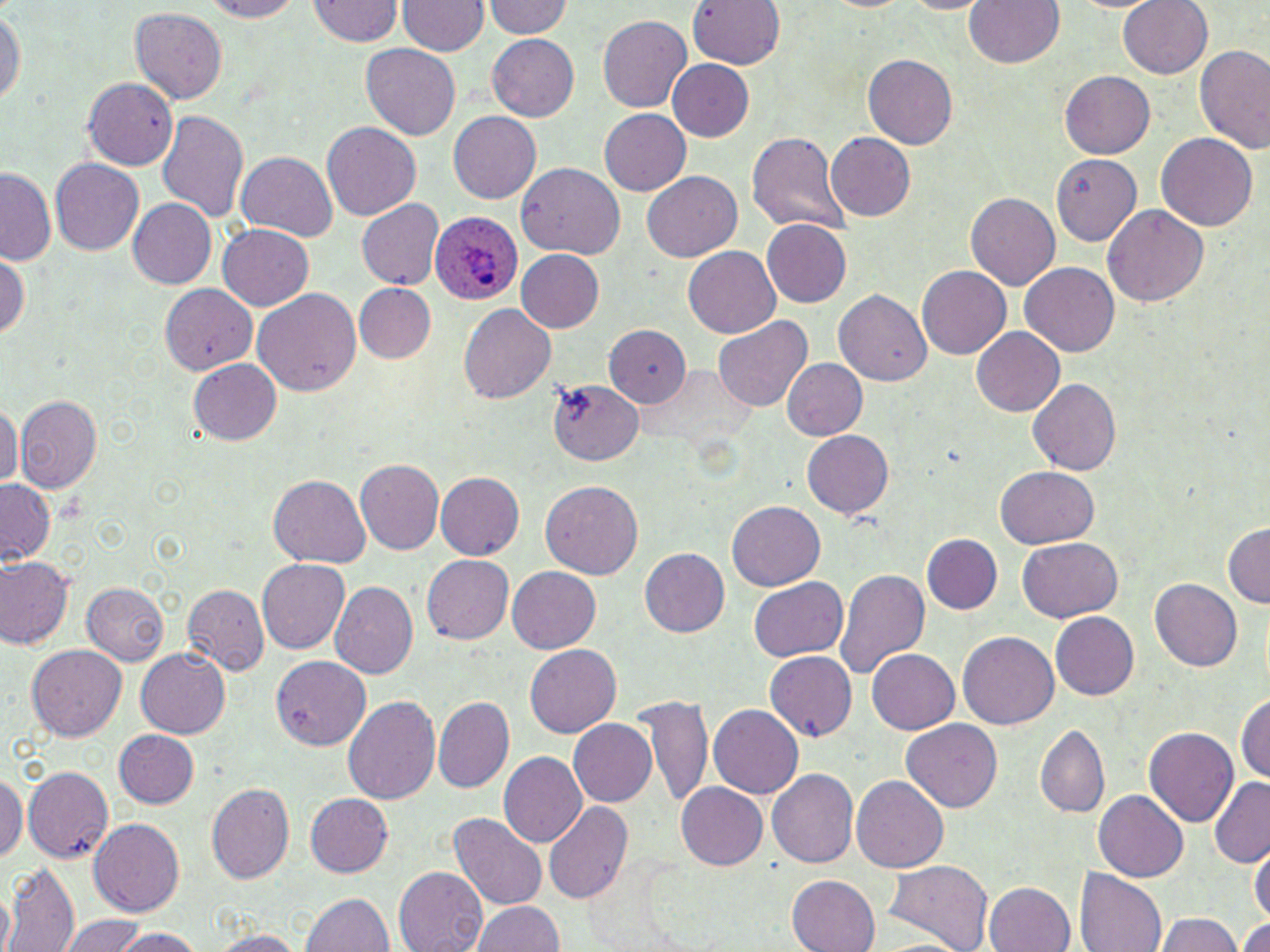
Summary:
  - Coordinate format: approximate bounding boxes as [x1, y1, x2, y2] in pixels
  - Uninfected red blood cell locations: [689, 0, 783, 68], [204, 1, 303, 21], [307, 1, 405, 46], [398, 1, 489, 56], [482, 1, 573, 38], [966, 1, 1065, 69], [1119, 1, 1213, 78], [899, 2, 996, 13], [0, 5, 24, 110], [130, 7, 228, 103], [597, 13, 692, 112], [486, 32, 579, 121], [360, 44, 461, 140], [1195, 44, 1270, 152], [864, 54, 959, 149], [667, 59, 754, 141], [1060, 70, 1154, 159], [80, 77, 179, 169], [599, 108, 692, 194], [157, 109, 248, 222], [449, 111, 542, 204], [322, 120, 421, 221], [746, 131, 850, 236], [826, 132, 915, 221], [1156, 133, 1258, 232], [237, 151, 339, 241], [1050, 154, 1143, 246], [51, 158, 144, 255], [516, 162, 623, 260], [1, 166, 55, 264], [643, 172, 741, 262], [965, 193, 1059, 290], [127, 197, 218, 289], [357, 199, 444, 290], [1104, 205, 1208, 307], [761, 219, 853, 307], [218, 224, 314, 310], [683, 246, 781, 339], [516, 249, 604, 332], [0, 251, 28, 340], [1020, 262, 1119, 356], [917, 266, 1010, 359], [159, 283, 258, 374], [354, 283, 435, 362], [253, 288, 361, 395], [835, 288, 931, 387], [459, 302, 557, 404], [712, 315, 812, 412], [605, 325, 690, 406], [972, 327, 1065, 417], [189, 358, 281, 445], [782, 358, 868, 440], [1027, 377, 1121, 475], [548, 378, 642, 464], [15, 395, 102, 492], [0, 400, 21, 488], [802, 430, 894, 519], [356, 461, 444, 554], [996, 465, 1099, 548], [435, 471, 525, 559], [269, 475, 371, 567], [0, 478, 54, 564], [541, 479, 643, 578], [726, 499, 825, 590], [1223, 521, 1269, 607], [922, 534, 1001, 613], [1018, 537, 1123, 622], [639, 547, 730, 636], [422, 554, 514, 643], [0, 557, 73, 649], [258, 559, 350, 654], [507, 565, 601, 652], [833, 568, 930, 681], [750, 576, 848, 661], [1151, 578, 1242, 671], [81, 581, 168, 665], [330, 581, 418, 678], [183, 585, 269, 674], [1051, 610, 1140, 699], [958, 629, 1058, 728], [25, 644, 127, 741], [524, 646, 621, 738], [136, 649, 230, 738], [867, 649, 959, 734], [765, 651, 857, 738], [271, 656, 371, 749], [638, 693, 712, 810], [433, 695, 514, 791], [1235, 695, 1269, 781], [342, 697, 439, 805], [709, 704, 803, 798], [568, 718, 656, 806], [901, 718, 1002, 813], [1036, 726, 1109, 817], [1145, 727, 1237, 825], [115, 729, 200, 808], [499, 752, 587, 847], [22, 766, 114, 866], [769, 769, 859, 869], [0, 770, 26, 864], [851, 774, 947, 872], [1208, 776, 1270, 865], [206, 782, 295, 884], [676, 782, 768, 869], [1092, 790, 1189, 882], [305, 792, 393, 877], [544, 800, 633, 904], [450, 813, 548, 909], [89, 818, 184, 915], [1249, 837, 1270, 926], [884, 860, 993, 952], [2, 863, 79, 951], [394, 867, 487, 952], [1075, 868, 1165, 952], [786, 874, 878, 952], [1244, 878, 1270, 952], [985, 882, 1073, 952], [0, 885, 15, 952], [300, 892, 395, 952], [473, 900, 562, 952], [1153, 913, 1243, 952], [59, 915, 149, 951], [1234, 916, 1270, 952], [114, 928, 202, 950], [207, 931, 307, 952]
  - Plasmodium ovale-infected red blood cell locations: [430, 212, 523, 306]
  - Slide-level diagnosis: Plasmodium ovale
  - Magnification: 1000x
  - Field of view: single
  - Modality: optical microscopy
  - Stain: May-Grünwald-Giemsa
  - Preparation: thin blood film
  - Image size: 1270×952 pixels